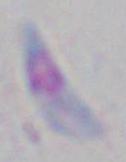

Summary:
  - Identification: Toxoplasma gondii
  - Modality: micrograph
  - Magnification: 1000x